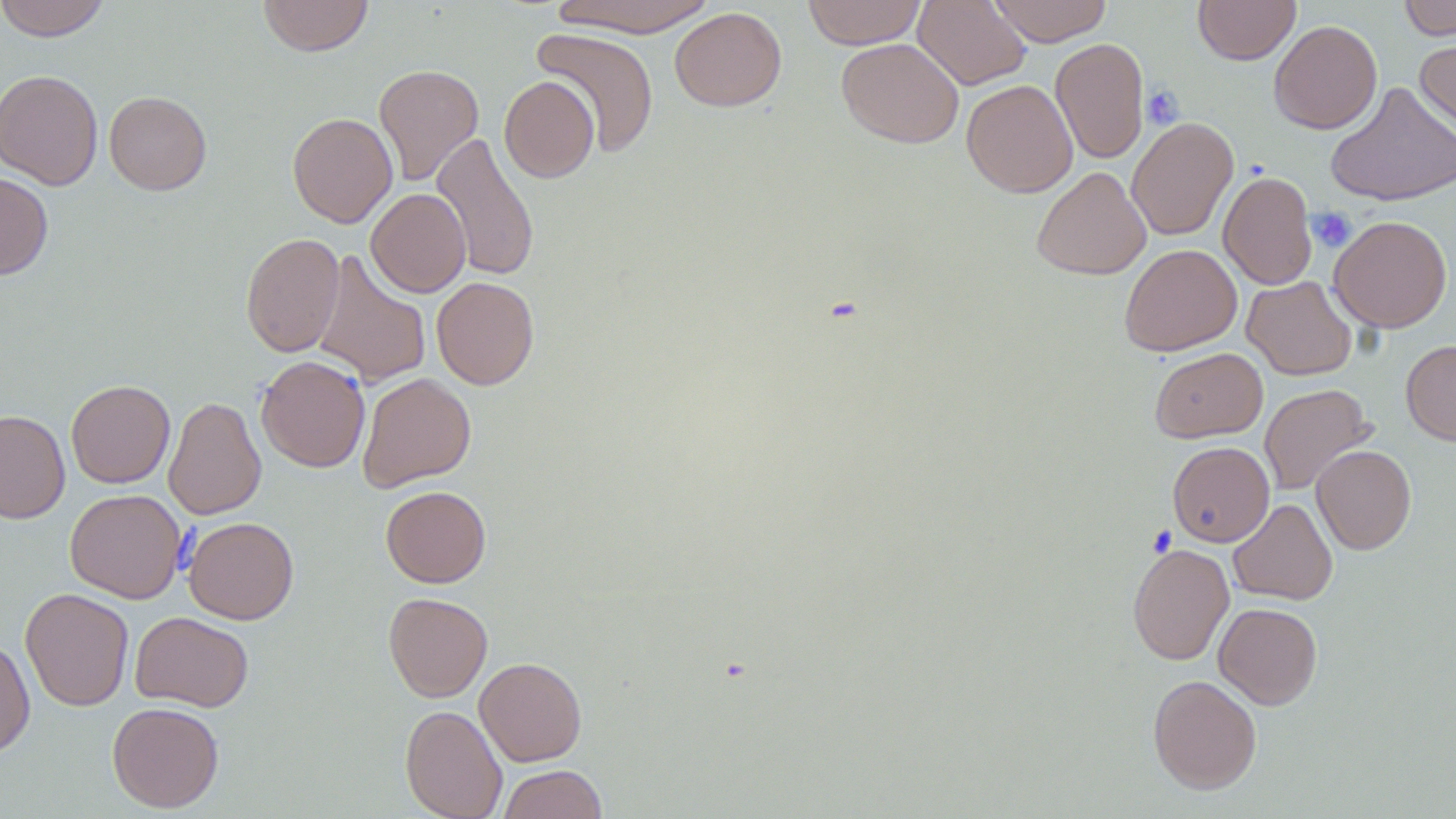

Summary:
  - Coordinate format: approximate bounding boxes as named x1/y1/x2/y2 corners in pixels
  - Platelet locations: (x1=1141, y1=85, x2=1184, y2=129), (x1=1307, y1=207, x2=1357, y2=252)
  - Uninfected red blood cell locations: (x1=0, y1=0, x2=111, y2=41), (x1=257, y1=0, x2=374, y2=56), (x1=548, y1=0, x2=718, y2=37), (x1=802, y1=0, x2=927, y2=49), (x1=913, y1=0, x2=1030, y2=90), (x1=988, y1=0, x2=1112, y2=46), (x1=1193, y1=0, x2=1300, y2=65), (x1=1399, y1=0, x2=1456, y2=40), (x1=669, y1=6, x2=787, y2=112), (x1=1268, y1=19, x2=1382, y2=134), (x1=532, y1=27, x2=660, y2=157), (x1=1414, y1=35, x2=1456, y2=142), (x1=1050, y1=37, x2=1149, y2=164), (x1=836, y1=38, x2=964, y2=148), (x1=373, y1=64, x2=484, y2=186), (x1=1, y1=69, x2=103, y2=190), (x1=499, y1=76, x2=600, y2=183), (x1=961, y1=79, x2=1078, y2=198), (x1=1325, y1=81, x2=1456, y2=207), (x1=104, y1=91, x2=212, y2=195), (x1=287, y1=113, x2=398, y2=228), (x1=1126, y1=117, x2=1238, y2=241), (x1=430, y1=131, x2=540, y2=282), (x1=1031, y1=166, x2=1152, y2=280), (x1=1218, y1=171, x2=1317, y2=290), (x1=0, y1=172, x2=53, y2=280), (x1=366, y1=188, x2=471, y2=297), (x1=1329, y1=215, x2=1452, y2=333), (x1=240, y1=232, x2=345, y2=357), (x1=1119, y1=243, x2=1242, y2=356), (x1=312, y1=250, x2=431, y2=388), (x1=1242, y1=275, x2=1357, y2=380), (x1=432, y1=277, x2=539, y2=390), (x1=1401, y1=339, x2=1456, y2=445), (x1=1150, y1=347, x2=1267, y2=443), (x1=256, y1=355, x2=371, y2=473), (x1=358, y1=373, x2=476, y2=492), (x1=66, y1=379, x2=175, y2=488), (x1=1259, y1=384, x2=1375, y2=495), (x1=163, y1=395, x2=265, y2=520), (x1=0, y1=410, x2=70, y2=524), (x1=1167, y1=441, x2=1275, y2=547), (x1=1311, y1=444, x2=1416, y2=554), (x1=381, y1=485, x2=491, y2=587), (x1=65, y1=489, x2=186, y2=603), (x1=1228, y1=498, x2=1337, y2=605), (x1=183, y1=516, x2=299, y2=624), (x1=1127, y1=543, x2=1234, y2=665), (x1=20, y1=588, x2=134, y2=711), (x1=383, y1=592, x2=493, y2=702), (x1=1213, y1=602, x2=1323, y2=709), (x1=130, y1=611, x2=254, y2=712), (x1=0, y1=638, x2=35, y2=759), (x1=474, y1=657, x2=587, y2=766), (x1=1148, y1=674, x2=1262, y2=794), (x1=107, y1=701, x2=224, y2=813), (x1=400, y1=704, x2=508, y2=819), (x1=497, y1=765, x2=608, y2=819)
  - Slide-level diagnosis: no evidence of blood parasites
  - Preparation: thin blood smear
  - Magnification: 1000x
  - Field of view: single
  - Image size: 1456×819 pixels
  - Stain: May-Grünwald-Giemsa
  - Modality: optical microscopy